Comment on the morphology of the red blood cells.
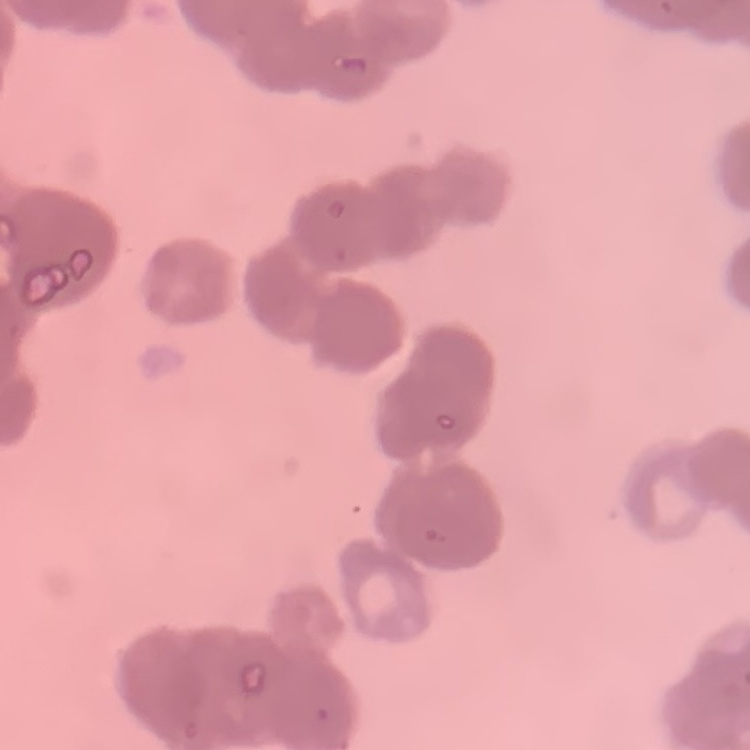
They show rouleaux formation.

preparation = thin blood smear
stain = Field's or Giemsa
image type = square crop of a larger photomicrograph